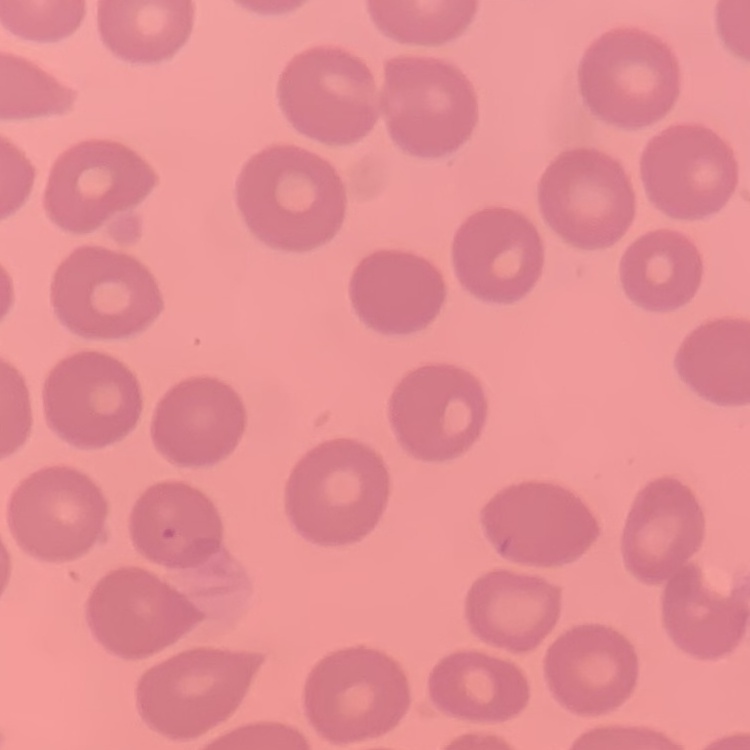
red_blood_cell_morphology: no rouleaux formation
preparation: thin blood smear
image_type: square crop of a larger photomicrograph
stain: Field's or Giemsa